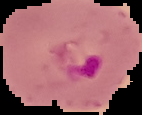

Summary:
  - Preparation: thin blood smear
  - Image size: 142×115 pixels
  - Image type: segmented cell region with the area outside set to black
  - Result: malaria parasites identified